Assess for Plasmodium parasites.
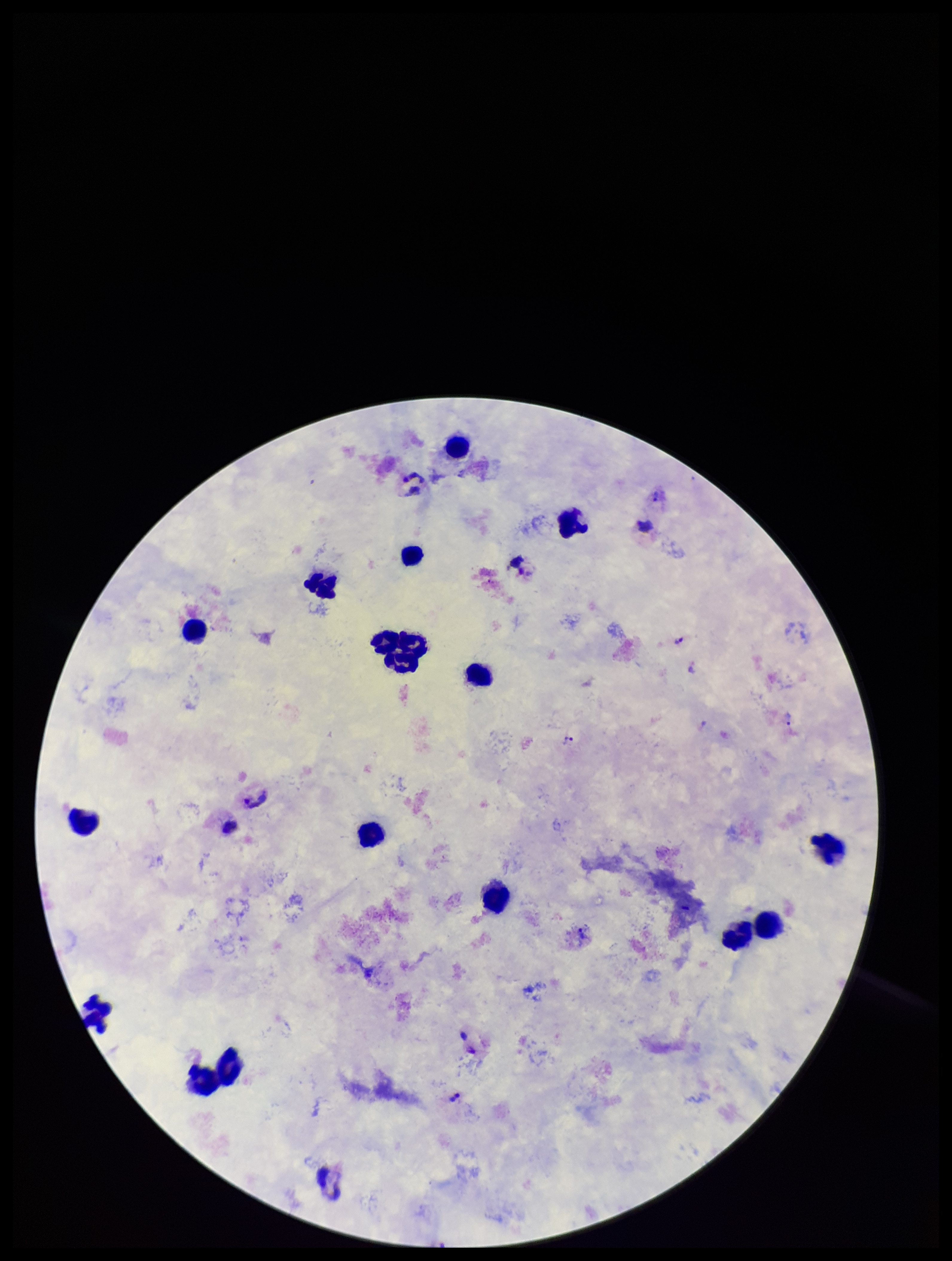
Identified.

Summary:
  - Preparation: thick blood smear
  - Parasite count: 5
  - Patient malaria status: infected
  - Leukocyte count: 15
  - Image size: 952×1261 pixels
  - Stain: Giemsa
  - Capture: smartphone photograph through the microscope eyepiece
  - Species reported for this patient: Plasmodium vivax
  - Field of view: single